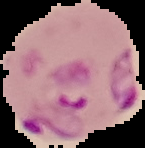
Image is 145×148 pixels. Cell region segmented out of the field of view; the surrounding area is masked to black. From a thin blood film. Malaria status: parasitized.